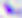

modality = photomicrograph
magnification = 400x
identification = Toxoplasma gondii